Give the extent of all Plasmodium vivax-infected red blood cells.
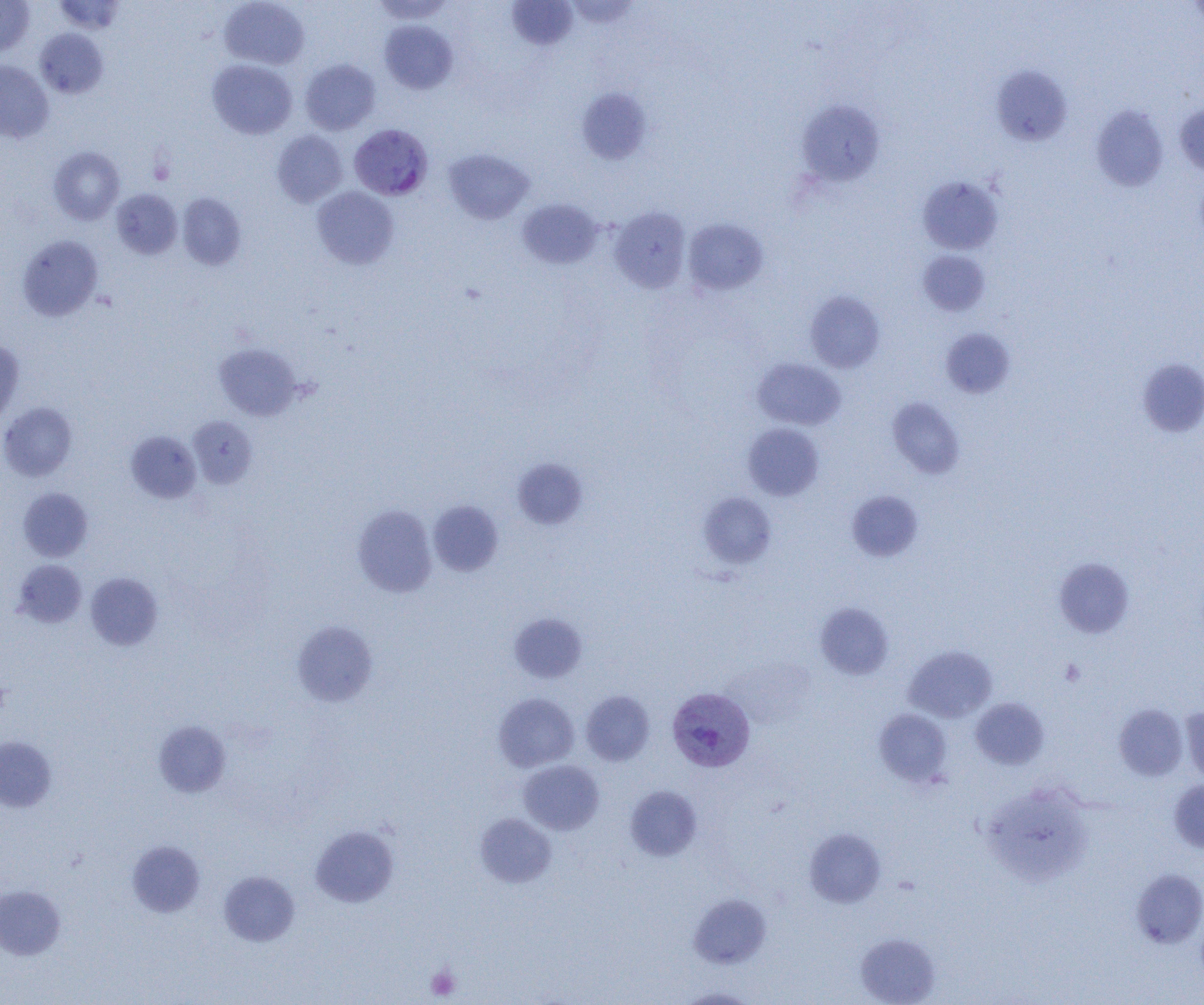
Approximate bounding boxes as (x1, y1, x2, y2) in pixels.
Plasmodium vivax-infected red blood cells: (349, 124, 433, 200), (667, 687, 755, 772).

slide-level diagnosis = Plasmodium vivax
uninfected red blood cell locations = approximate bounding boxes as (x1, y1, x2, y2) in pixels: (0, 0, 35, 56), (53, 0, 126, 34), (370, 0, 456, 23), (506, 0, 578, 50), (219, 1, 310, 69), (379, 20, 457, 94), (35, 29, 109, 98), (207, 59, 297, 139), (300, 59, 381, 135), (0, 60, 53, 143), (991, 65, 1073, 146), (577, 88, 651, 165), (796, 100, 885, 186), (1175, 101, 1204, 177), (1091, 105, 1168, 191), (272, 130, 347, 207), (49, 146, 125, 225), (443, 148, 534, 224), (918, 176, 1002, 255), (312, 186, 399, 269), (111, 188, 183, 259), (177, 193, 246, 270), (517, 198, 604, 269), (608, 207, 691, 293), (683, 218, 768, 296), (17, 235, 103, 321), (917, 250, 990, 315), (805, 291, 885, 373), (941, 328, 1015, 398), (0, 340, 24, 424), (213, 343, 303, 420), (753, 358, 846, 430), (1137, 358, 1204, 438), (887, 397, 966, 478), (0, 402, 78, 481), (188, 416, 257, 488), (743, 423, 824, 501), (125, 430, 201, 503), (513, 458, 588, 529), (18, 487, 93, 562), (846, 490, 923, 562), (698, 492, 777, 568), (428, 500, 503, 576), (352, 505, 437, 597), (1054, 558, 1134, 638), (13, 559, 87, 628), (85, 573, 163, 650), (815, 602, 894, 679), (509, 613, 587, 683), (292, 620, 378, 706), (903, 645, 998, 723), (581, 691, 654, 765), (493, 693, 579, 772), (970, 698, 1049, 769), (1114, 704, 1188, 781), (1181, 706, 1204, 786), (874, 709, 952, 786), (154, 721, 231, 797), (0, 737, 56, 811), (518, 760, 604, 835), (1169, 779, 1204, 852), (625, 785, 702, 861), (985, 793, 1095, 894), (475, 813, 557, 888), (310, 826, 398, 906), (804, 828, 886, 908), (127, 841, 205, 917), (1131, 868, 1204, 948), (219, 871, 300, 946), (0, 885, 65, 960), (688, 893, 771, 969), (856, 933, 940, 1005), (677, 987, 759, 1004)
modality = light microscopy
platelet locations = approximate bounding boxes as (x1, y1, x2, y2) in pixels: (1060, 659, 1085, 686), (0, 677, 11, 718), (426, 966, 460, 1000)
field of view = single
preparation = thin blood film
magnification = 1000x
image size = 1204×1005 pixels